Comment on the morphology of the erythrocytes.
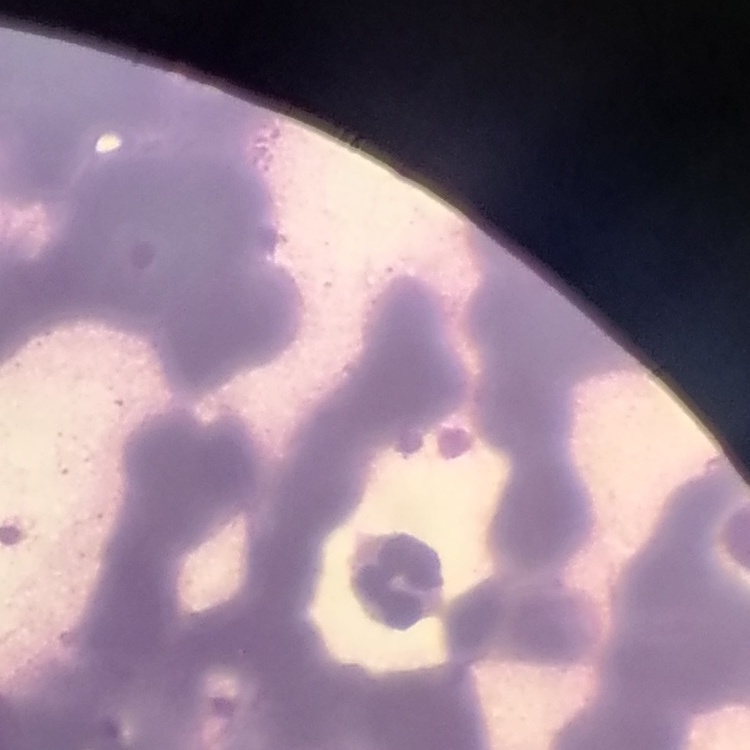

Rouleaux formation.

Summary:
  - Image type: square crop of a larger photomicrograph
  - Stain: Field's or Giemsa
  - Preparation: thin peripheral smear